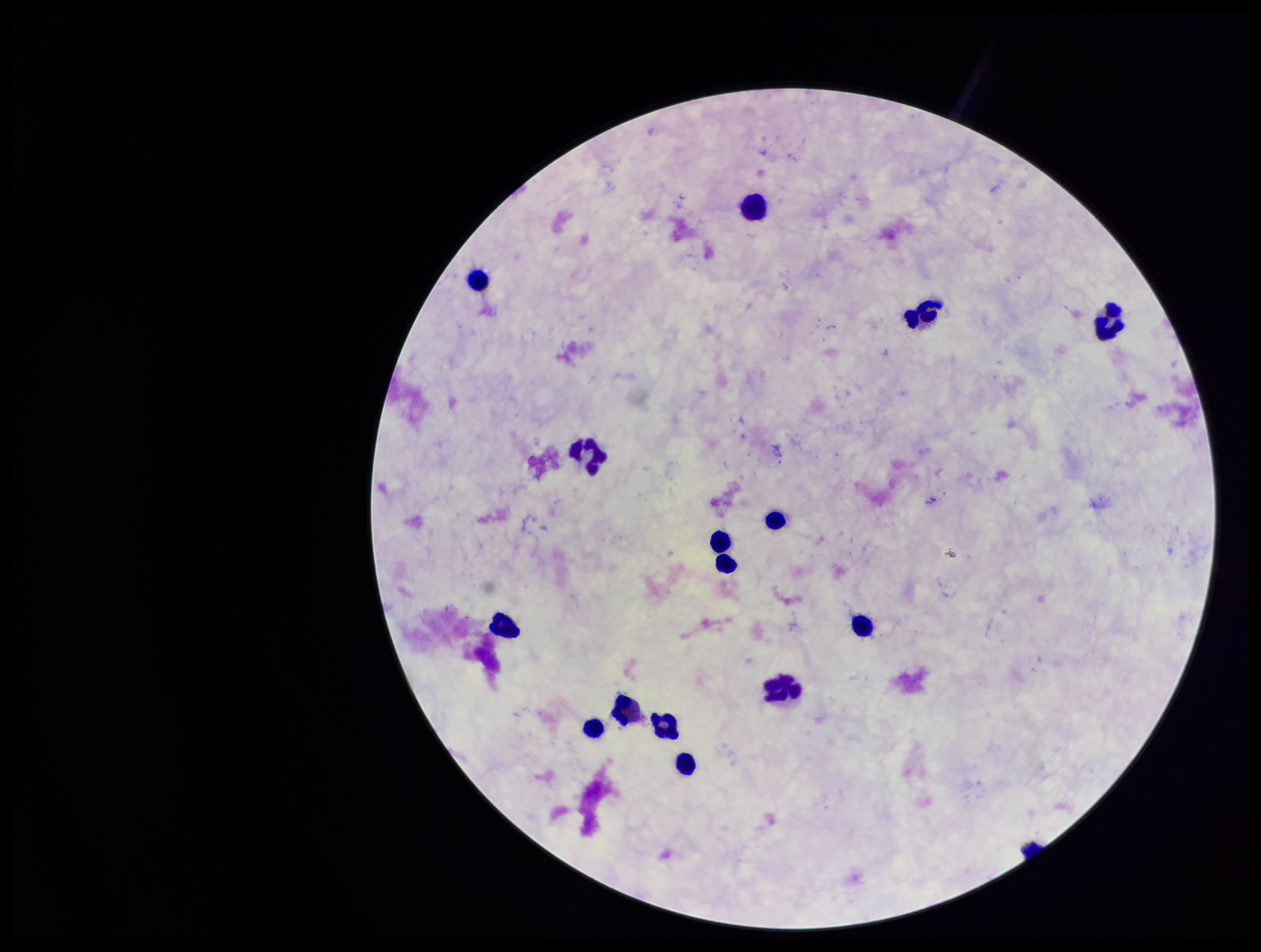 Parasite count: 0. Single field of view. Leukocyte count: 15. Patient malaria status: negative. Photographed through the microscope eyepiece with a smartphone camera. Image is 1261×952 pixels. Plasmodium parasites: none seen. Giemsa stain. Preparation: thick.